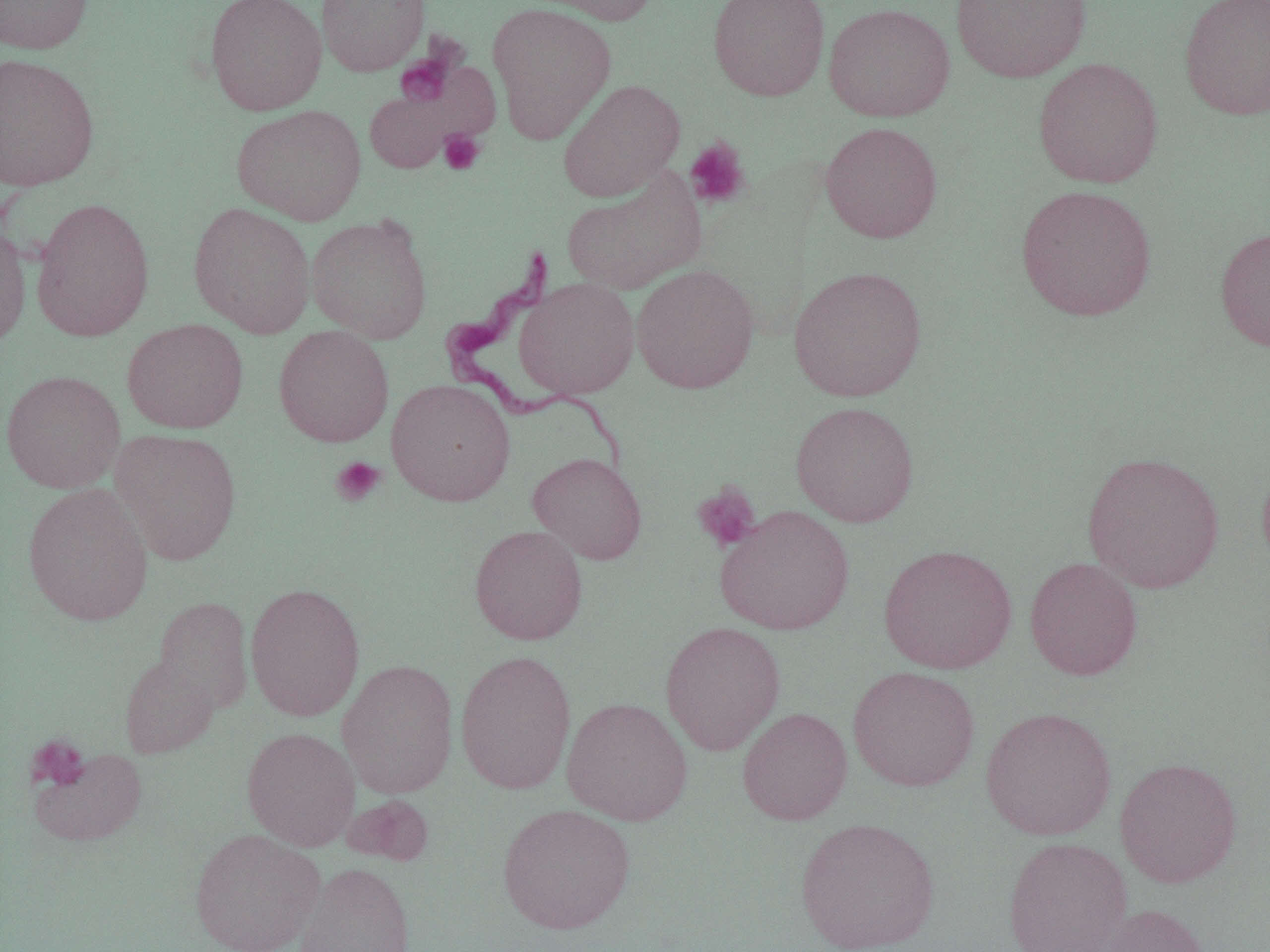
{
  "slide_level_diagnosis": "Trypanosoma brucei",
  "field_of_view": "single",
  "preparation": "thin blood smear",
  "magnification": "1000x",
  "platelet_locations": "approximate bounding boxes as [x1, y1, x2, y2] in pixels: [396, 53, 455, 107], [438, 129, 485, 175], [684, 137, 751, 210], [331, 456, 386, 506], [692, 483, 761, 552], [25, 734, 90, 791]",
  "trypanosoma_brucei_locations": "approximate bounding boxes as [x1, y1, x2, y2] in pixels: [435, 236, 626, 481]",
  "image_size": "1270×952 pixels",
  "uninfected_red_blood_cell_locations": "approximate bounding boxes as [x1, y1, x2, y2] in pixels: [0, 0, 93, 54], [204, 0, 327, 116], [316, 0, 430, 76], [525, 0, 660, 26], [707, 0, 830, 101], [951, 0, 1091, 83], [1179, 0, 1270, 121], [823, 2, 956, 122], [487, 3, 616, 142], [0, 53, 100, 192], [1033, 57, 1164, 189], [558, 79, 685, 202], [231, 104, 366, 225], [819, 121, 943, 243], [561, 171, 704, 295], [1015, 185, 1157, 321], [30, 197, 155, 341], [188, 202, 316, 337], [306, 215, 433, 343], [0, 221, 32, 349], [1215, 226, 1270, 353], [631, 264, 760, 394], [789, 265, 927, 401], [515, 277, 640, 399], [122, 318, 249, 434], [273, 325, 394, 447], [0, 370, 125, 493], [386, 379, 516, 506], [790, 401, 919, 527], [110, 428, 241, 565], [1081, 450, 1225, 593], [528, 451, 647, 564], [1256, 458, 1270, 576], [22, 483, 154, 626], [715, 505, 855, 635], [469, 524, 588, 645], [879, 543, 1017, 674], [1024, 556, 1143, 681], [245, 582, 365, 720], [153, 596, 253, 713], [660, 621, 786, 756], [455, 648, 577, 795], [119, 654, 219, 758], [337, 659, 459, 798], [847, 666, 980, 792], [562, 697, 693, 826], [980, 706, 1117, 841], [737, 707, 853, 825], [241, 727, 361, 851], [29, 747, 146, 847], [1115, 756, 1242, 888], [343, 795, 435, 867], [497, 802, 636, 934], [794, 817, 940, 952], [189, 828, 324, 952], [1002, 836, 1133, 952], [295, 861, 416, 952], [1096, 903, 1212, 952]",
  "modality": "light microscopy"
}